Locate every leukocyte (white blood cell).
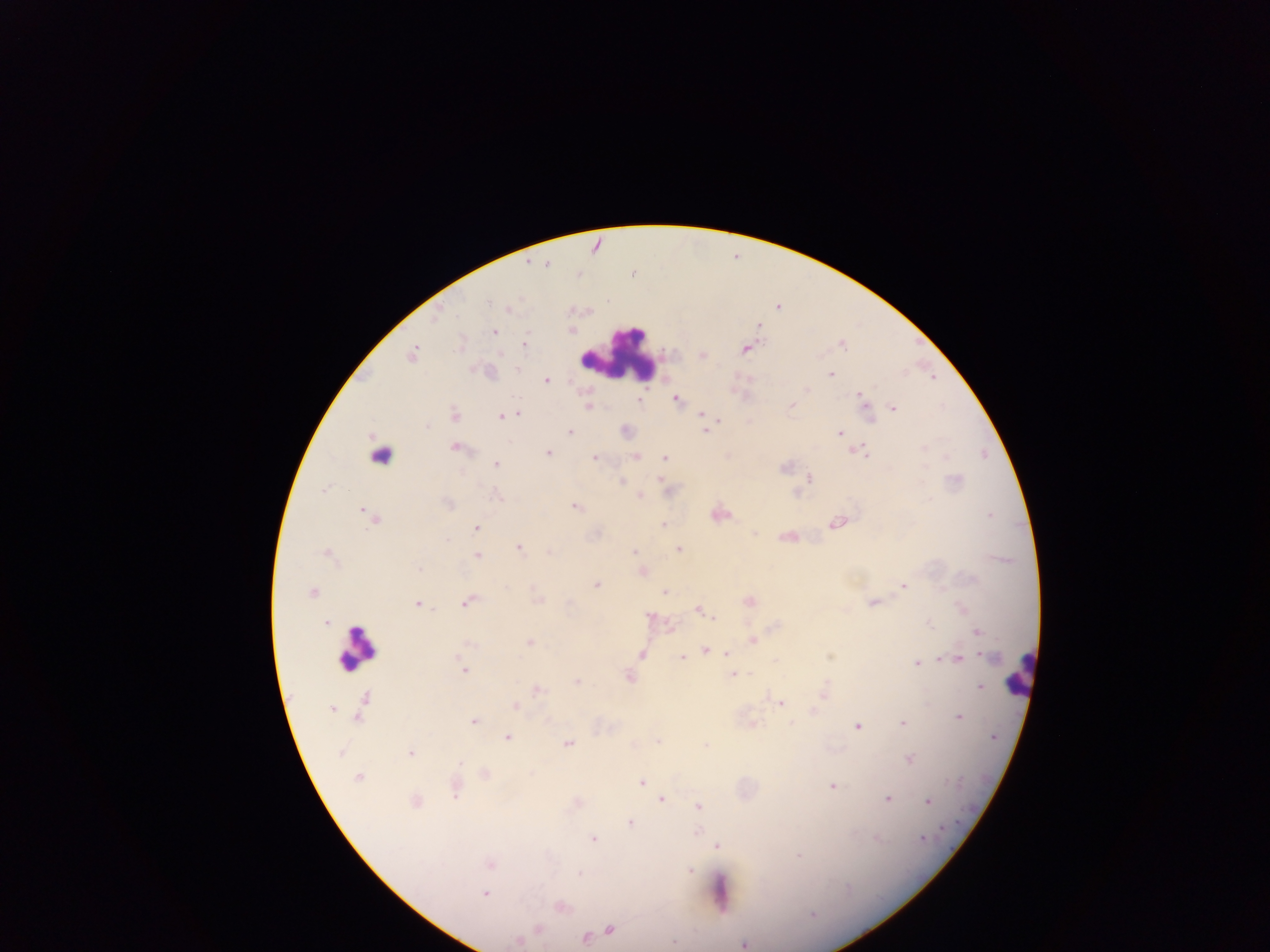

Approximate centers as [x, y] in pixels.
Leukocytes: [620, 353], [370, 461], [357, 649], [1019, 673], [719, 892].

Plasmodium parasite locations: [545, 264], [778, 306], [508, 309], [758, 325], [570, 329], [494, 331], [523, 345], [744, 349], [411, 353], [703, 354], [518, 368], [829, 374], [546, 380], [859, 395], [676, 398], [639, 401], [791, 405], [588, 406], [892, 407], [518, 413], [701, 415], [454, 416], [502, 416], [705, 430], [569, 432], [839, 433], [455, 448], [855, 450], [549, 453], [867, 454], [635, 456], [665, 457], [594, 458], [496, 464], [808, 478], [661, 480], [621, 481], [639, 496], [576, 506], [717, 513], [366, 514], [374, 518], [835, 524], [663, 525], [476, 527], [787, 536], [519, 547], [678, 549], [634, 551], [549, 552], [326, 553], [477, 555], [642, 571], [596, 584], [903, 585], [312, 592], [664, 592], [538, 599], [748, 601], [467, 602], [873, 602], [417, 604], [698, 610], [715, 618], [327, 623], [977, 631], [752, 639], [530, 642], [705, 649], [727, 652], [641, 653], [682, 656], [957, 659], [916, 662], [463, 671], [733, 674], [629, 676], [576, 681], [979, 687], [536, 689], [823, 693], [363, 701], [780, 702], [515, 705], [331, 706], [813, 711], [958, 717], [473, 722], [751, 724], [902, 724], [856, 726], [507, 737], [656, 741], [567, 743], [410, 753], [909, 760], [484, 774], [359, 777], [641, 781], [831, 786], [455, 789], [661, 798], [887, 799], [415, 801], [927, 802], [698, 807], [630, 822], [697, 830], [592, 838], [716, 845], [799, 854], [490, 864], [688, 870], [485, 892], [560, 906], [537, 928], [608, 930], [584, 938], [518, 941], [742, 944]. Image is 1270×952 pixels. Single field of view. Collected in Ghana. Photographed through a microscope with a mobile-phone camera. Thick blood smear.